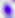
Toxoplasma gondii is shown. 400x magnification. Photomicrograph.